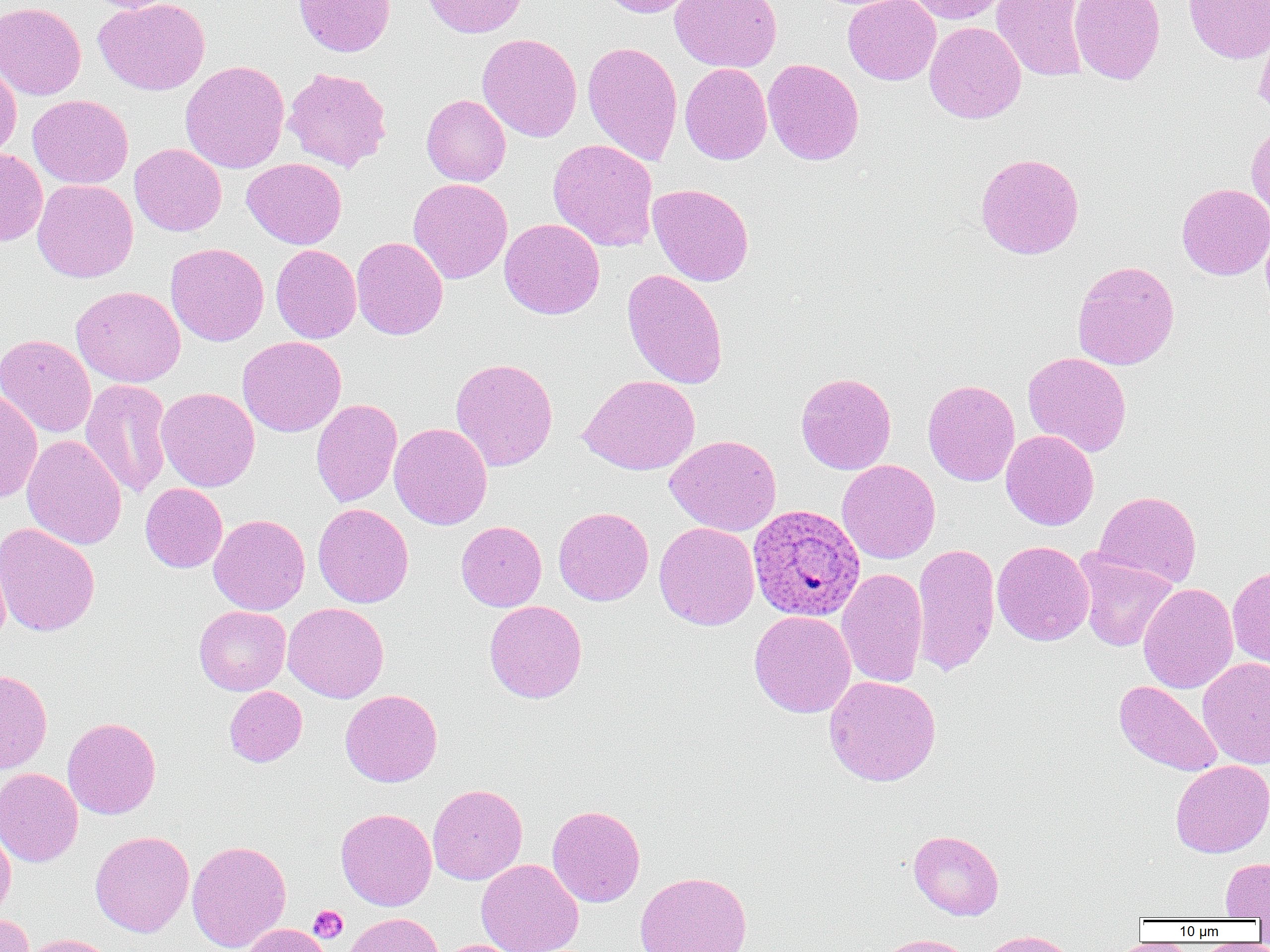

Summary:
  - Coordinate format: approximate bounding boxes as [x1, y1, x2, y2] in pixels
  - Uninfected red blood cell locations: [82, 0, 185, 13], [93, 0, 210, 95], [293, 0, 396, 57], [421, 0, 528, 38], [596, 0, 698, 17], [670, 0, 782, 72], [843, 0, 941, 85], [905, 0, 1010, 24], [991, 0, 1089, 82], [1069, 0, 1166, 85], [1183, 0, 1270, 64], [0, 1, 86, 100], [1254, 20, 1270, 120], [924, 21, 1026, 124], [477, 33, 582, 142], [582, 40, 683, 165], [763, 58, 864, 166], [180, 60, 290, 173], [0, 61, 22, 162], [680, 63, 772, 164], [283, 67, 392, 172], [28, 94, 133, 189], [422, 95, 511, 185], [1246, 122, 1270, 219], [548, 138, 658, 251], [130, 143, 226, 236], [0, 148, 48, 246], [975, 152, 1085, 260], [243, 158, 347, 249], [32, 178, 139, 283], [407, 178, 512, 284], [648, 183, 754, 286], [1176, 183, 1270, 280], [499, 218, 605, 319], [351, 236, 448, 340], [165, 243, 269, 346], [271, 244, 361, 343], [1072, 260, 1180, 370], [622, 268, 728, 389], [71, 285, 186, 387], [0, 334, 97, 438], [237, 336, 347, 437], [1023, 352, 1132, 457], [450, 358, 558, 471], [796, 372, 896, 474], [579, 374, 700, 475], [80, 379, 173, 499], [922, 379, 1020, 486], [155, 387, 260, 492], [0, 389, 42, 503], [311, 399, 402, 507], [389, 422, 493, 530], [1000, 429, 1099, 530], [22, 434, 127, 550], [665, 434, 782, 536], [836, 459, 940, 564], [140, 483, 227, 572], [1094, 490, 1202, 588], [313, 503, 414, 608], [553, 506, 654, 605], [208, 514, 311, 615], [456, 521, 547, 611], [654, 521, 759, 630], [0, 523, 100, 637], [992, 541, 1094, 646], [912, 543, 1000, 676], [1074, 551, 1178, 652], [1227, 565, 1270, 670], [836, 568, 928, 688], [1138, 583, 1238, 693], [484, 600, 587, 703], [283, 602, 389, 703], [194, 605, 291, 695], [749, 610, 856, 718], [1197, 657, 1270, 769], [0, 669, 52, 774], [824, 675, 941, 786], [1114, 680, 1223, 777], [224, 686, 307, 767], [340, 689, 443, 787], [62, 717, 161, 819], [1170, 759, 1270, 858], [0, 767, 83, 867], [428, 783, 527, 885], [547, 805, 645, 907], [335, 808, 437, 910], [0, 824, 16, 922], [90, 830, 194, 937], [908, 830, 1004, 920], [187, 839, 292, 952], [476, 858, 584, 952], [1220, 858, 1270, 920], [635, 871, 753, 952], [0, 912, 35, 952], [344, 913, 442, 952], [242, 923, 333, 952], [977, 930, 1080, 952], [20, 933, 119, 952], [872, 933, 978, 952], [436, 939, 529, 952]
  - Platelet locations: [309, 905, 347, 943]
  - Plasmodium ovale-infected red blood cell locations: [748, 504, 865, 621]
  - Slide-level diagnosis: Plasmodium ovale
  - Field of view: one of a larger specimen
  - Modality: light microscopy
  - Magnification: 1000x
  - Preparation: thin blood film
  - Image size: 1270×952 pixels